Evaluate for malaria.
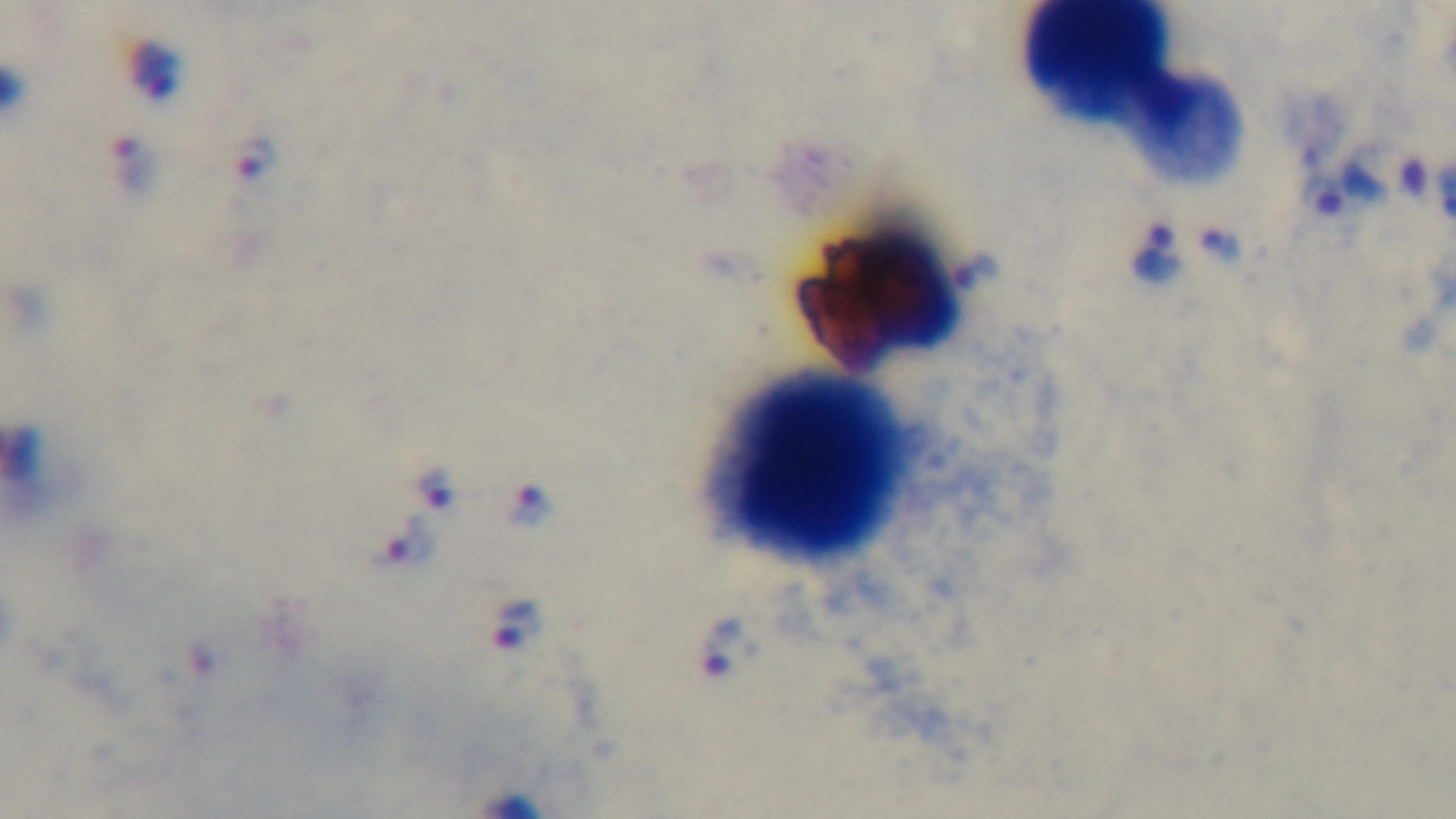
Positive.

Summary:
  - Capture: mounted 4K digital camera
  - Stain: Giemsa
  - Preparation: thick blood film
  - Field of view: one from the slide
  - Objective: 100x oil immersion
  - Modality: light microscopy